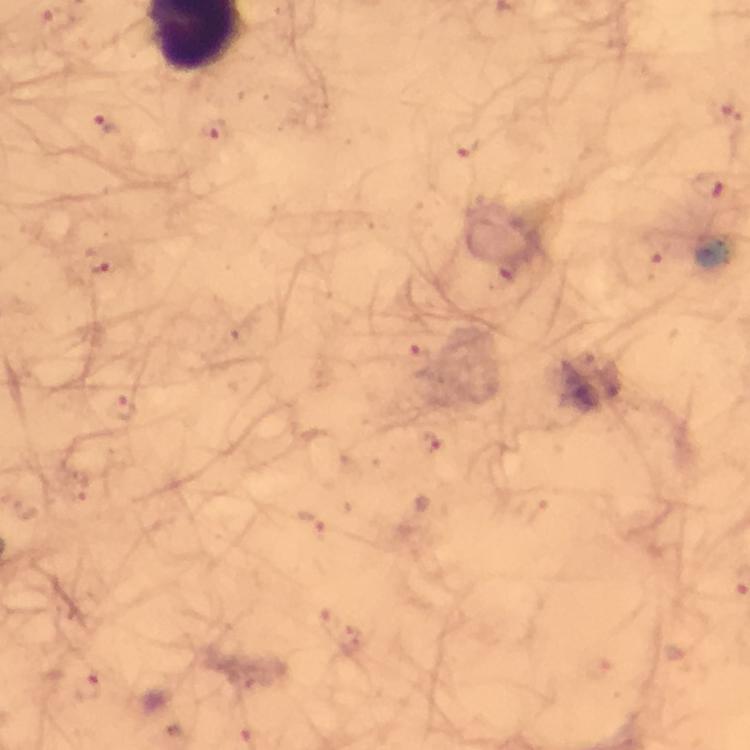
{
  "image_size": "750×750 pixels",
  "context": "from a malaria diagnostic workup",
  "magnification": "100x",
  "cropped_from": "one field of view",
  "immersion_oil": "used",
  "stain": "Giemsa",
  "capture": "smartphone mounted on the microscope",
  "preparation": "thick smear",
  "plasmodium_parasite_locations": "approximate object centers, in pixels from the top-left corner: (x=104, y=127), (x=214, y=131), (x=464, y=143), (x=708, y=185), (x=654, y=251), (x=104, y=266), (x=421, y=366), (x=120, y=410), (x=429, y=441), (x=313, y=526), (x=86, y=686)"
}